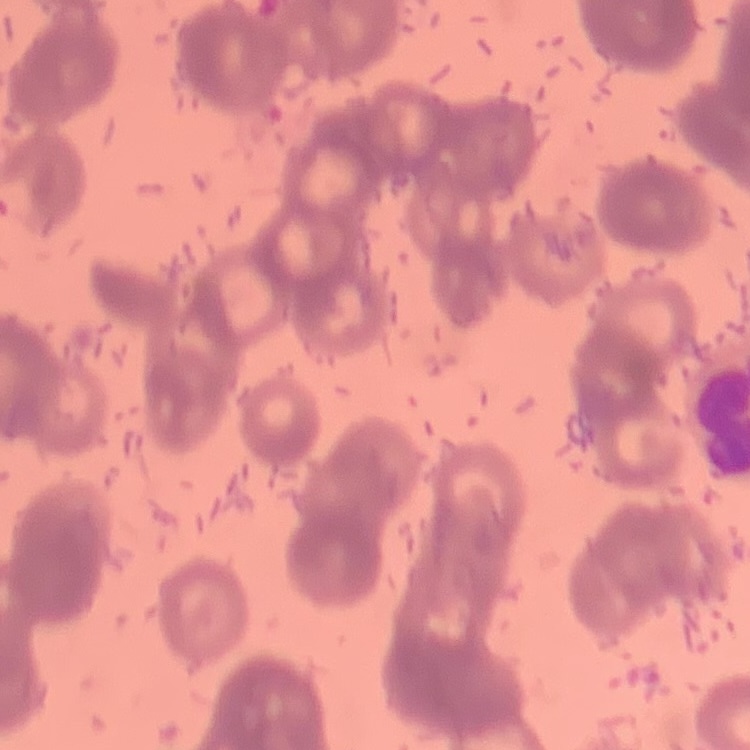
The erythrocytes show rouleaux formation. Stained with either Field's or Giemsa. Thin blood smear. Square crop of a larger photomicrograph.